State which parasite is depicted.
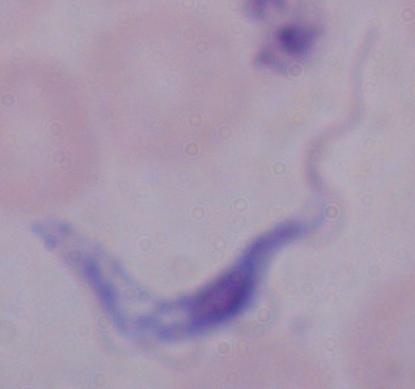
This is a trypanosome.

{
  "modality": "micrograph",
  "magnification": "1000x"
}